Locate every leukocyte (white blood cell).
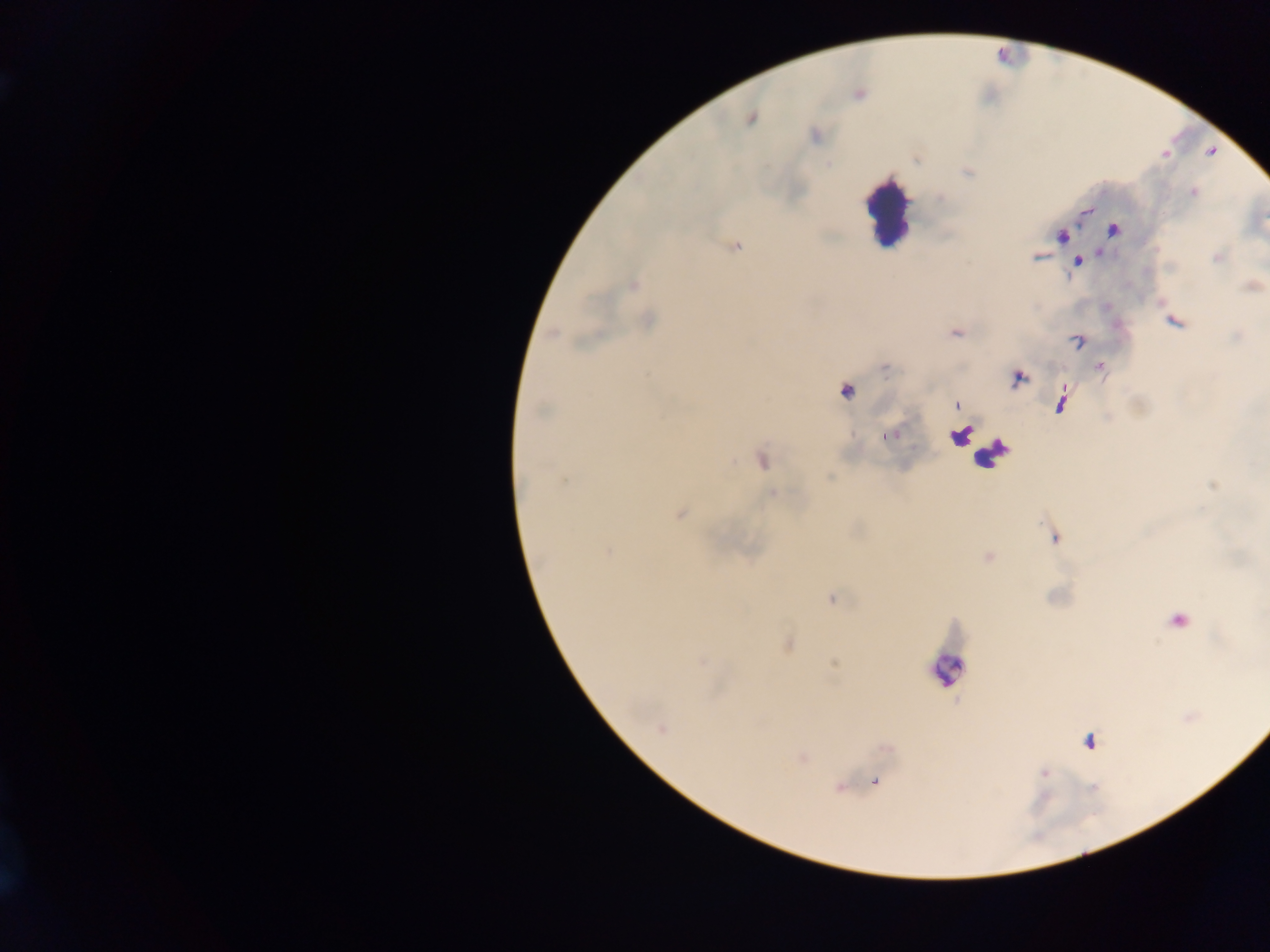

Approximate centers as [x, y] in pixels.
Leukocytes: [888, 212], [962, 434], [990, 453], [948, 668].

capture = mobile-phone photograph through a microscope
country = Ghana
malaria parasite locations = approximate centers as [x, y] in pixels: [751, 118], [1193, 192], [1112, 231], [736, 246], [1218, 257], [1078, 263], [633, 285], [648, 320], [1175, 322], [553, 333], [956, 333], [1078, 341], [1100, 367], [1017, 379], [846, 392], [1061, 403], [956, 405], [540, 411], [891, 435], [762, 461], [830, 477], [563, 481], [772, 493], [679, 514], [1055, 537], [607, 552], [832, 598], [1179, 621], [789, 644], [702, 662], [662, 729], [1089, 741], [1044, 773], [876, 783]
image size = 1270×952 pixels
preparation = thick blood film
field of view = single